Outline each Plasmodium ovale-infected red blood cell.
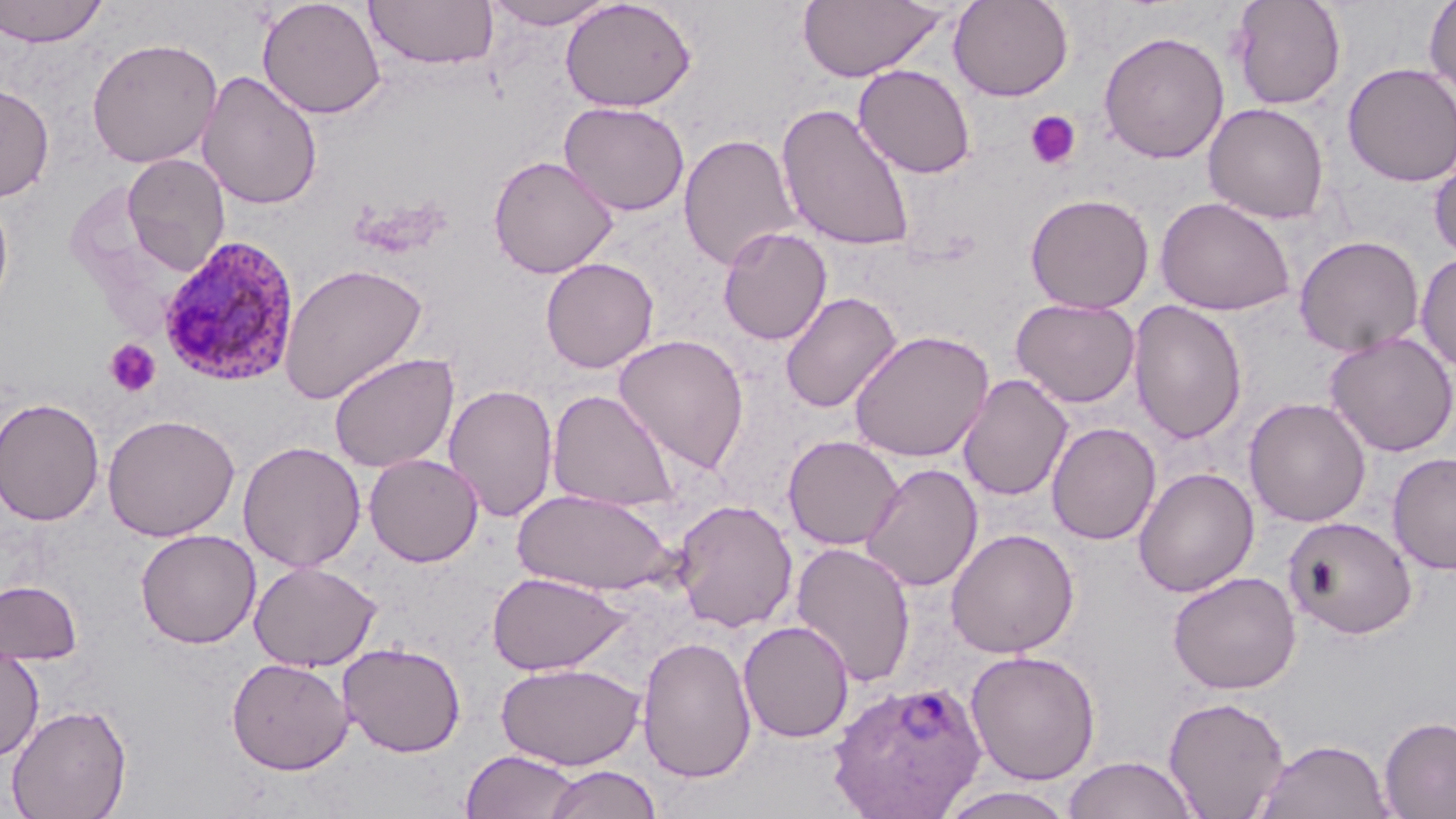

Approximate bounding boxes as (x1,y1)-(x2,y2) corner pairs in pixels.
Plasmodium ovale-infected red blood cells: (157,235)-(301,387), (827,678)-(987,818).

slide-level diagnosis = Plasmodium ovale
field of view = one of a larger specimen
image size = 1456×819 pixels
preparation = thin blood smear
uninfected red blood cell locations = approximate bounding boxes as (x1,y1)-(x2,y2) corner pairs in pixels: (0,0)-(109,48), (257,0)-(386,119), (363,0)-(499,70), (481,0)-(618,29), (560,0)-(696,112), (949,0)-(1073,101), (1229,0)-(1347,110), (1424,0)-(1456,103), (797,1)-(949,82), (1098,30)-(1230,164), (86,37)-(223,168), (1342,62)-(1456,187), (853,65)-(976,179), (196,69)-(323,211), (0,82)-(54,202), (559,101)-(690,216), (777,103)-(916,252), (1203,103)-(1329,224), (677,133)-(801,271), (1429,147)-(1456,264), (122,154)-(231,276), (488,155)-(619,278), (0,188)-(14,322), (1024,192)-(1154,314), (1154,196)-(1295,316), (718,226)-(832,345), (1294,235)-(1425,357), (1416,252)-(1456,373), (540,257)-(659,373), (278,263)-(428,405), (779,292)-(902,413), (1010,297)-(1140,408), (1128,300)-(1248,445), (848,329)-(994,462), (1324,331)-(1456,457), (613,333)-(750,475), (328,351)-(459,473), (958,374)-(1073,502), (443,384)-(559,522), (547,388)-(681,513), (0,397)-(105,526), (1244,397)-(1371,527), (102,413)-(240,542), (1047,422)-(1161,545), (782,435)-(904,550), (238,441)-(366,572), (1387,452)-(1456,575), (364,453)-(484,567), (860,463)-(983,592), (1133,467)-(1259,597), (513,488)-(675,595), (671,499)-(798,632), (1285,516)-(1417,639), (136,528)-(261,649), (945,528)-(1079,658), (790,541)-(916,687), (249,560)-(381,671), (1167,570)-(1302,694), (487,571)-(630,676), (0,580)-(82,665), (738,620)-(854,743), (636,635)-(757,784), (339,642)-(466,758), (0,644)-(44,763), (965,649)-(1101,784), (226,657)-(353,775), (496,661)-(645,770), (1163,695)-(1291,818), (6,702)-(132,819), (1378,715)-(1456,819), (1255,738)-(1395,819), (460,749)-(581,818), (1062,756)-(1199,819), (542,764)-(663,819), (937,787)-(1077,818)
magnification = 1000x
stain = May-Grünwald-Giemsa
platelet locations = approximate bounding boxes as (x1,y1)-(x2,y2) corner pairs in pixels: (1025,110)-(1081,170), (104,339)-(160,397)
modality = optical microscopy